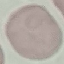

result = negative for malaria parasites
preparation = thin smear
image type = automatically extracted cell patch, resized to 64 × 64 pixels
stain = Giemsa
capture = smartphone camera at the microscope eyepiece